Identify the blood parasite species.
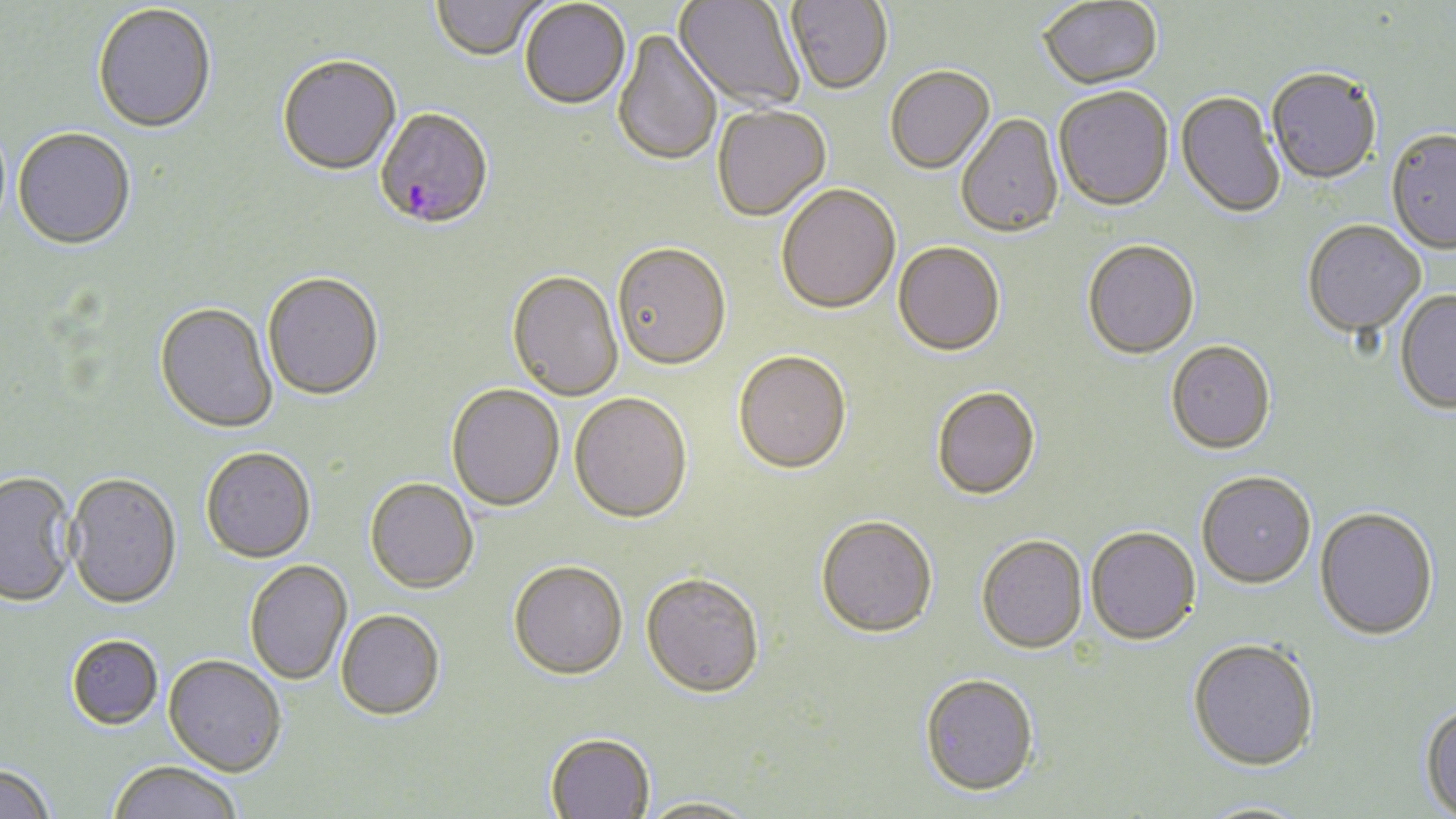
Plasmodium falciparum.

{
  "field_of_view": "one of a larger specimen",
  "stain": "May-Grünwald-Giemsa",
  "magnification": "1000x",
  "modality": "optical microscopy",
  "plasmodium_falciparum_infected_red_blood_cell_locations": "approximate bounding boxes as (x1,y1)-(x2,y2) corner pairs in pixels: (374,110)-(493,233)",
  "preparation": "thin blood film",
  "image_size": "1456×819 pixels",
  "uninfected_red_blood_cell_locations": "approximate bounding boxes as (x1,y1)-(x2,y2) corner pairs in pixels: (785,0)-(893,97), (432,1)-(544,64), (674,1)-(805,114), (1039,1)-(1163,92), (519,2)-(631,112), (92,4)-(217,135), (613,30)-(722,169), (277,58)-(402,178), (886,68)-(996,176), (1267,70)-(1381,186), (1054,89)-(1174,214), (1175,93)-(1285,220), (712,107)-(831,223), (955,115)-(1064,240), (12,128)-(136,250), (1386,131)-(1456,255), (776,186)-(901,316), (1302,222)-(1426,339), (1082,242)-(1200,361), (893,244)-(1005,359), (612,245)-(731,373), (507,272)-(623,402), (262,275)-(383,403), (1395,291)-(1456,415), (154,304)-(278,434), (1166,343)-(1276,456), (733,353)-(851,477), (446,386)-(564,513), (931,389)-(1041,503), (569,395)-(692,526), (200,448)-(316,564), (0,470)-(78,606), (66,473)-(182,609), (1196,473)-(1317,591), (365,480)-(479,595), (1315,508)-(1439,642), (815,518)-(938,641), (1086,528)-(1200,647), (976,537)-(1088,656), (244,560)-(352,685), (509,563)-(628,683), (640,576)-(764,702), (336,611)-(445,723), (65,634)-(163,729), (1187,639)-(1320,772), (162,656)-(286,778), (919,676)-(1038,800), (1420,701)-(1456,818), (545,734)-(655,818), (107,761)-(243,819), (0,763)-(55,819), (635,797)-(761,818), (1193,800)-(1317,819)"
}